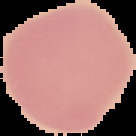

Summary:
  - Preparation: thin blood film
  - Result: negative for malaria parasites
  - Image size: 136×136 pixels
  - Image type: segmented cell region on a black background